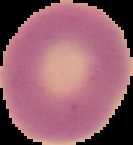
malaria status = uninfected
preparation = thin blood smear
image size = 133×145 pixels
image type = segmented cell region on a black background